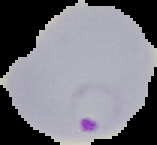
Segmented cell region on a black background. From a thin blood smear. Result: malaria parasites identified. Image is 157×145 pixels.